Report the malaria status of this cell.
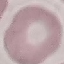
Uninfected.

image type = automatically extracted cell patch, resized to 64 × 64 pixels
preparation = thin blood film
stain = Giemsa
capture = smartphone through the microscope eyepiece